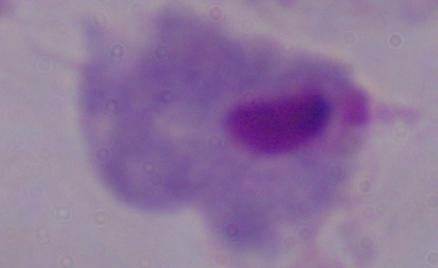
magnification = 1000x
modality = micrograph
identification = trichomonad